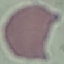

malaria status = uninfected
stain = Giemsa
preparation = thin blood film
image type = automatically extracted cell patch, resized to 64 × 64 pixels
capture = smartphone through the microscope eyepiece